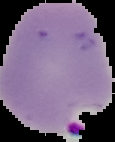 Malaria status: parasitized. From a thin blood film. Segmented cell region on a black background. Image is 115×142 pixels.